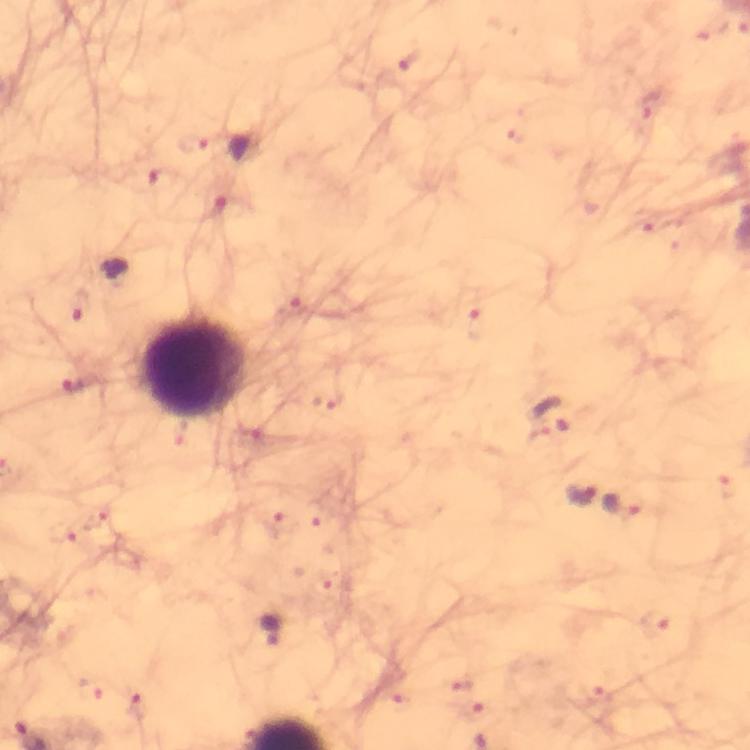
Approximate centers as [x, y] in pixels. Malaria parasite locations: [194, 142], [112, 273], [80, 381], [550, 414], [579, 497], [624, 506], [271, 628]. Leukocyte locations: [193, 368]. Thick smear. Immersion oil applied. Photographed through the microscope with a smartphone camera. 100x magnification. Image is 750×750 pixels. Cropped region of a single field of view. Giemsa stain. From a diagnostic examination for malaria.